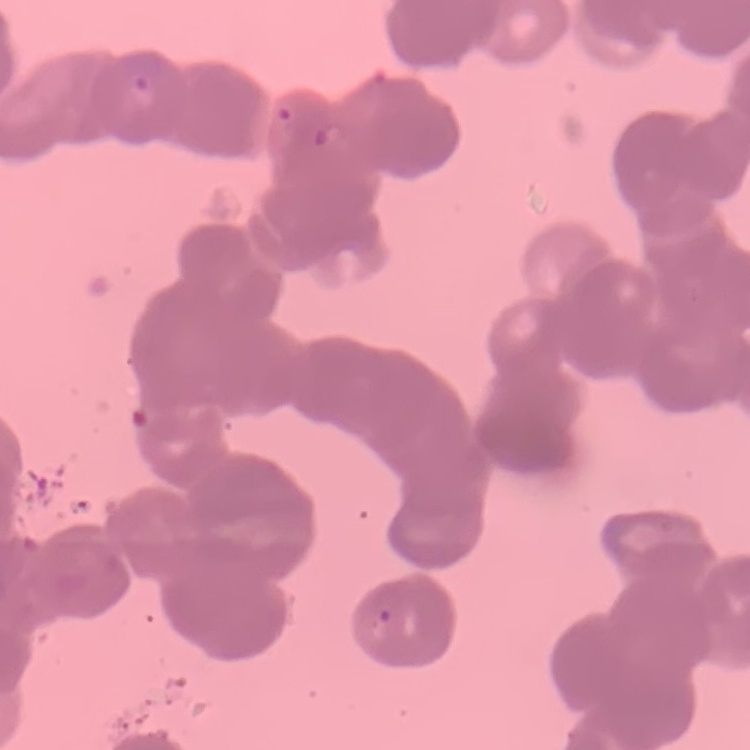

The erythrocytes show rouleaux formation. One tile cut from a larger photomicrograph. Thin blood film. Field's or Giemsa stain.